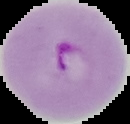

image_size: 130×124 pixels
preparation: thin blood film
image_type: cell region segmented out of the field of view; surrounding area masked to black
malaria_status: parasitized